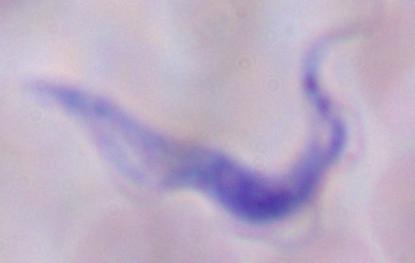

Micrograph. A trypanosome is seen. 1000x magnification.